Report the malaria status of this cell.
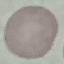

It is uninfected.

capture = smartphone through the microscope eyepiece
preparation = thin smear
image type = automatically extracted cell patch, resized to 64 × 64 pixels
stain = Giemsa